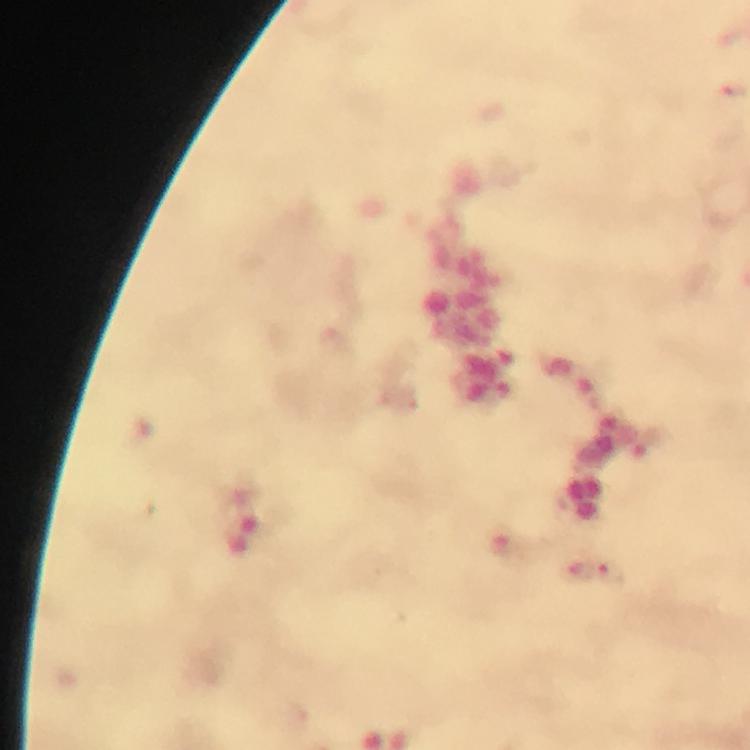
Approximate centers as [x, y] in pixels.
Summary:
  - Plasmodium parasite locations: [733, 90], [578, 572], [612, 580]
  - Immersion oil: applied
  - Magnification: 100x
  - Cropped from: one field of view
  - Stain: Giemsa
  - Context: from a malaria diagnostic workup
  - Capture: smartphone photograph through a microscope
  - Image size: 750×750 pixels
  - Preparation: thick blood smear